Give the position of every leukocyte visible.
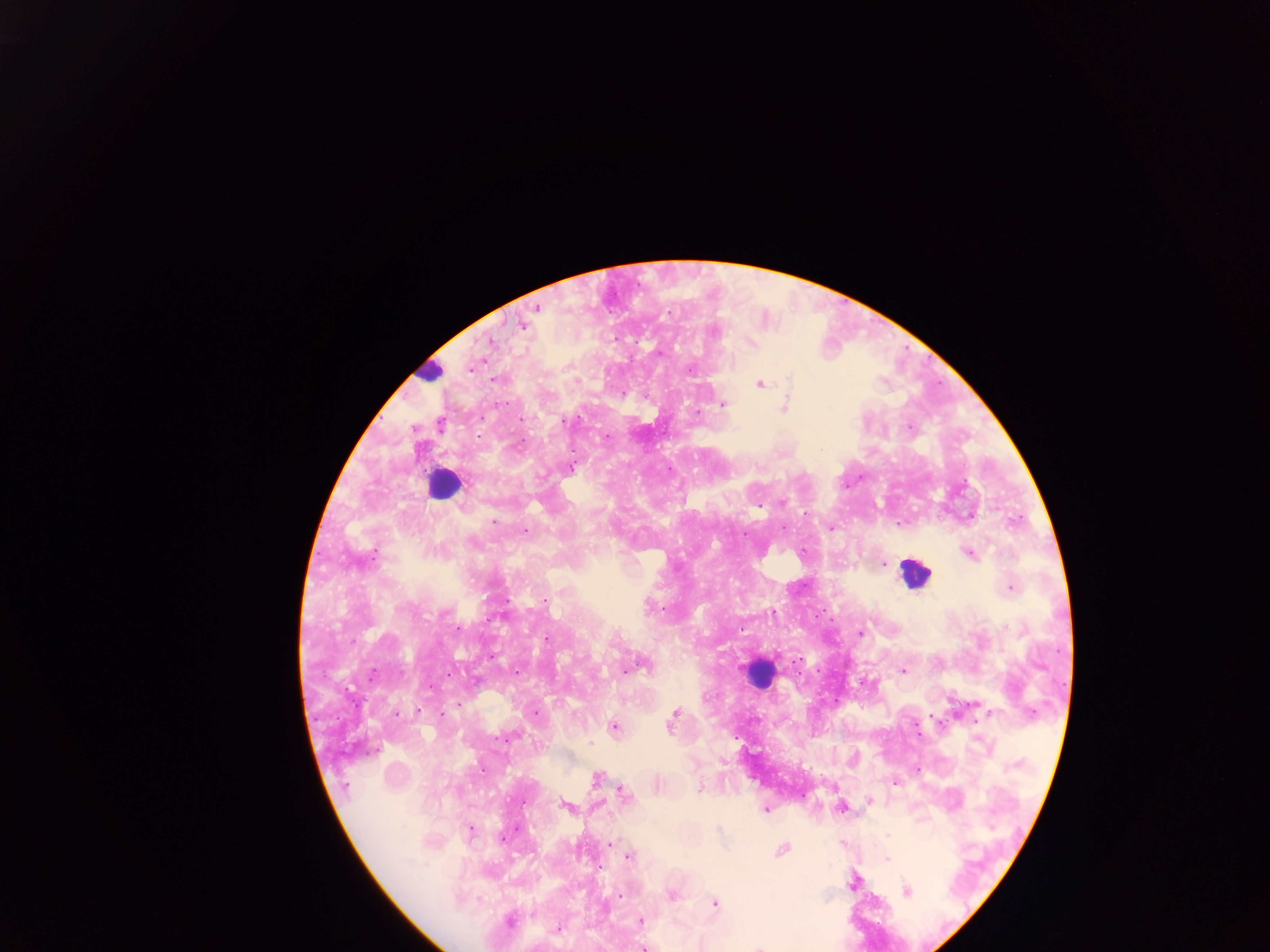
Approximate centers as (x, y) in pixels.
Leukocytes: (428, 372), (443, 483), (914, 575), (764, 674).

Malaria parasite locations: (536, 306), (522, 325), (715, 332), (751, 344), (793, 379), (497, 380), (761, 384), (790, 385), (784, 402), (722, 405), (520, 418), (911, 427), (570, 469), (684, 500), (493, 518), (832, 528), (525, 529), (966, 553), (882, 564), (1011, 588), (545, 601), (650, 606), (458, 629), (860, 631), (644, 663), (517, 670), (624, 671), (904, 671), (371, 674), (417, 710), (675, 713), (987, 715), (670, 722), (613, 725), (513, 736), (591, 740), (723, 762), (594, 777), (894, 784), (701, 786), (346, 788), (622, 794), (870, 801), (565, 806), (765, 809), (719, 829), (470, 831), (887, 836), (506, 837), (610, 845), (783, 850), (629, 857), (886, 859), (852, 885), (908, 893), (620, 894), (671, 896), (715, 904), (511, 917), (640, 920), (557, 928), (642, 946), (757, 946). Thick blood smear. Photographed through a microscope with a mobile-phone camera. Sample from Ghana. Image is 1270×952 pixels. Single field of view.